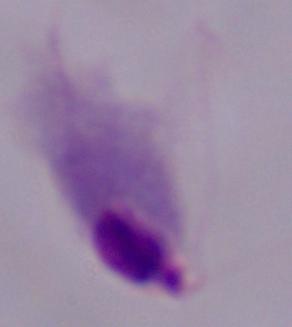
{
  "magnification": "1000x",
  "identification": "trichomonad",
  "modality": "micrograph"
}